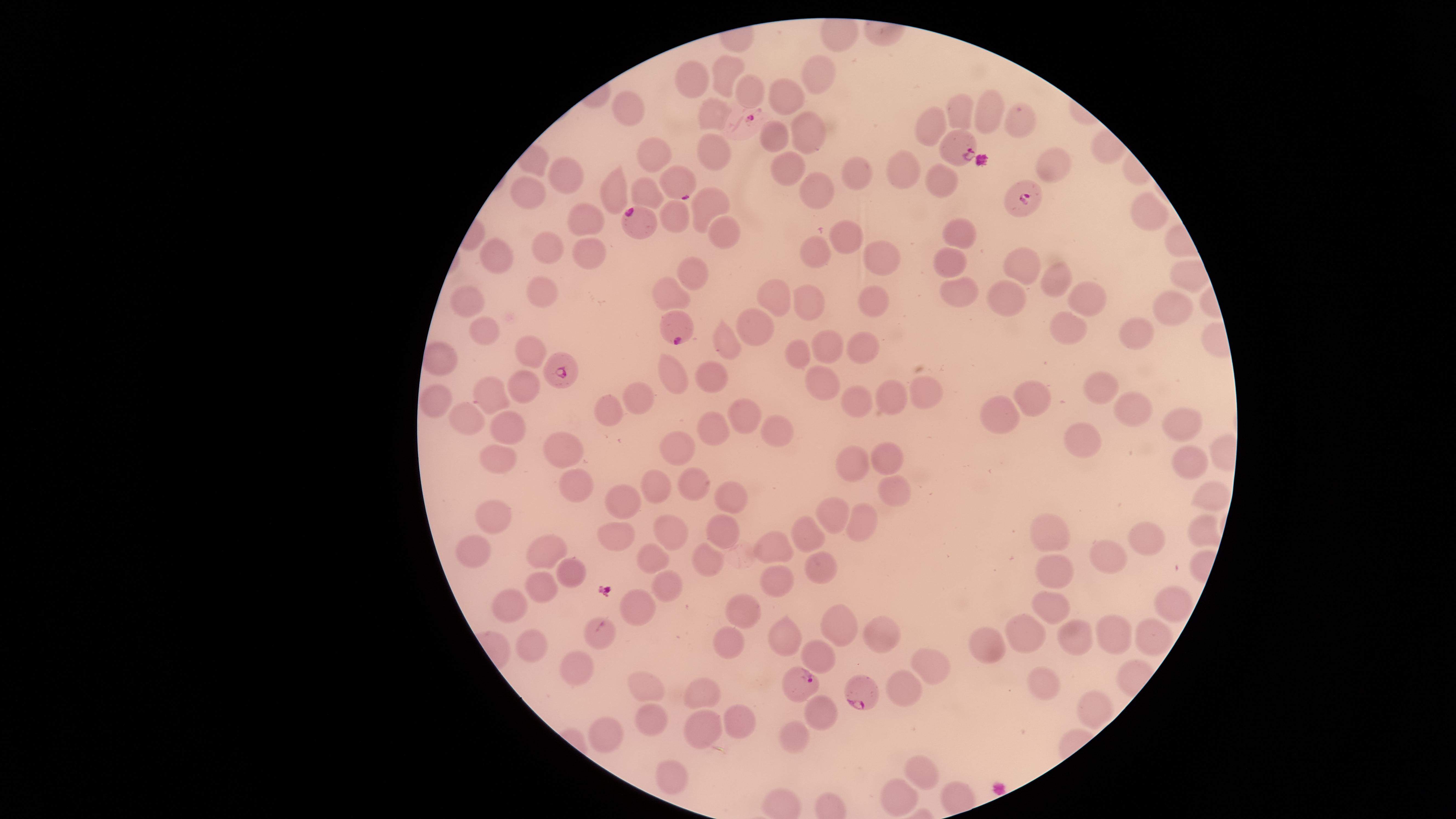
Approximate marker points, in pixels from the top-left corner. Parasitized red blood cells: (x=742, y=120), (x=963, y=149), (x=679, y=179), (x=1019, y=200), (x=639, y=218), (x=675, y=326), (x=562, y=364), (x=797, y=685), (x=862, y=694). Uninfected red blood cells: (x=720, y=71), (x=819, y=73), (x=691, y=75), (x=742, y=86), (x=792, y=96), (x=631, y=106), (x=955, y=107), (x=990, y=107), (x=1018, y=115), (x=716, y=119), (x=930, y=121), (x=810, y=129), (x=772, y=137), (x=714, y=152), (x=660, y=156), (x=1053, y=165), (x=789, y=166), (x=905, y=167), (x=943, y=172), (x=568, y=173), (x=853, y=173), (x=817, y=188), (x=530, y=189), (x=612, y=190), (x=645, y=195), (x=710, y=203), (x=582, y=215), (x=1143, y=216), (x=679, y=217), (x=722, y=224), (x=969, y=235), (x=845, y=236), (x=554, y=248), (x=589, y=248), (x=811, y=249), (x=500, y=253), (x=880, y=253), (x=948, y=256), (x=1024, y=266), (x=695, y=268), (x=1057, y=278), (x=955, y=285), (x=538, y=288), (x=671, y=290), (x=1085, y=294), (x=768, y=295), (x=1007, y=296), (x=873, y=298), (x=817, y=299), (x=471, y=300), (x=1168, y=309), (x=759, y=322), (x=479, y=329), (x=1067, y=330), (x=1129, y=331), (x=725, y=342), (x=825, y=343), (x=863, y=343), (x=798, y=351), (x=529, y=352), (x=438, y=356), (x=713, y=379), (x=676, y=382), (x=823, y=382), (x=523, y=385), (x=1103, y=387), (x=491, y=392), (x=927, y=392), (x=1035, y=392), (x=642, y=393), (x=887, y=396), (x=440, y=401), (x=851, y=402), (x=1139, y=408), (x=743, y=410), (x=472, y=411), (x=612, y=411), (x=1002, y=414), (x=1190, y=417), (x=509, y=424), (x=715, y=425), (x=770, y=430), (x=1086, y=439), (x=562, y=444), (x=678, y=444), (x=884, y=456), (x=503, y=460), (x=1191, y=460), (x=850, y=463), (x=660, y=482), (x=577, y=486), (x=701, y=488), (x=891, y=488), (x=1214, y=496), (x=619, y=497), (x=734, y=498), (x=835, y=513), (x=498, y=515), (x=861, y=523), (x=1203, y=528), (x=673, y=530), (x=718, y=531), (x=807, y=532), (x=617, y=533), (x=1051, y=536), (x=1146, y=540), (x=773, y=543), (x=469, y=547), (x=544, y=551), (x=1109, y=553), (x=706, y=555), (x=652, y=559), (x=821, y=562), (x=1055, y=567), (x=568, y=573), (x=781, y=576), (x=662, y=581), (x=544, y=590), (x=635, y=602), (x=1052, y=602), (x=1167, y=602), (x=507, y=605), (x=743, y=609), (x=840, y=619), (x=878, y=626), (x=1022, y=631), (x=598, y=632), (x=1113, y=634), (x=783, y=635), (x=1079, y=638), (x=1153, y=639), (x=533, y=642), (x=727, y=644), (x=990, y=648), (x=822, y=655), (x=936, y=666), (x=573, y=667), (x=909, y=685), (x=648, y=689), (x=1044, y=689), (x=700, y=690), (x=1089, y=709), (x=817, y=714), (x=654, y=720), (x=738, y=720), (x=704, y=728), (x=610, y=736), (x=795, y=738), (x=924, y=773), (x=672, y=776), (x=903, y=796). One field of view of the specimen. Image is 1456×819 pixels. Species: Plasmodium falciparum. Circular visible region. Giemsa-stained preparation. Presence: malaria parasites detected. Photographed with a smartphone camera through the microscope eyepiece. Thin blood smear.